Assess this cell for malaria.
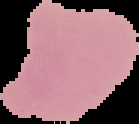
Uninfected.

preparation = thin blood film
image size = 139×124 pixels
image type = cell region segmented out of the field of view; surrounding area masked to black